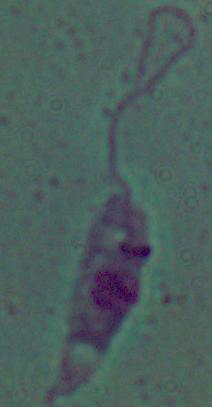

Summary:
  - Magnification: 1000x
  - Modality: photomicrograph
  - Identification: Leishmania